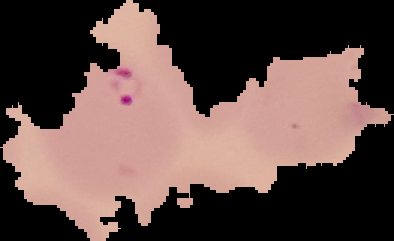 From a thin blood film. Malaria status: parasitized. Image is 394×241 pixels. The area outside the segmented cell region is set to black.